Evaluate for malaria.
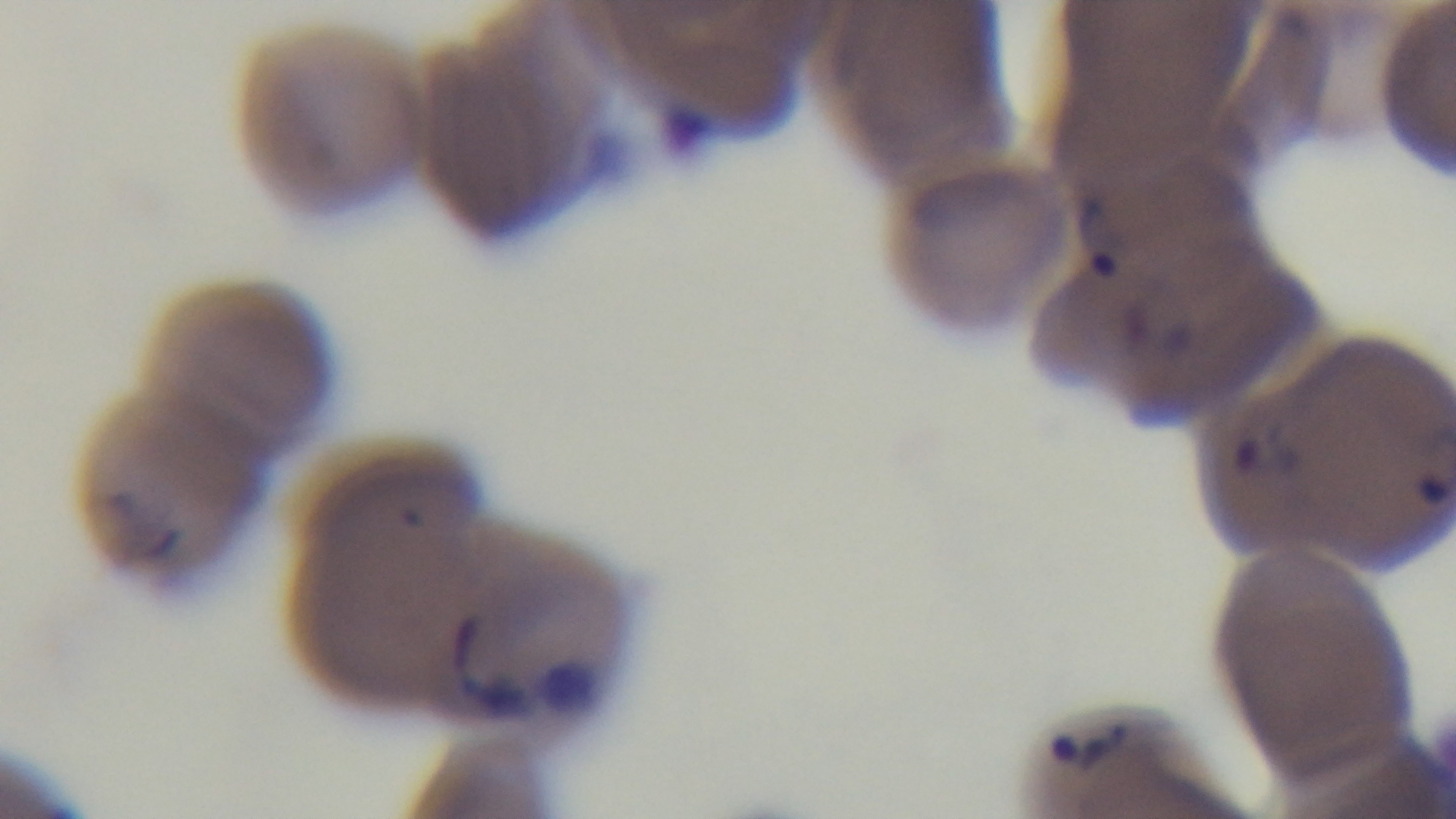

Positive.

Oil-immersion objective, 100x. Mounted 4K digital camera. Photomicrograph. Preparation: thin. Giemsa stain. One field from the slide.